State which cell type is depicted.
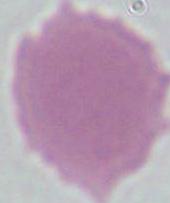
This is an erythrocyte.

modality = micrograph
magnification = 1000x